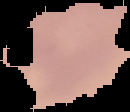
Summary:
  - Image size: 130×112 pixels
  - Preparation: thin blood smear
  - Malaria status: uninfected
  - Image type: segmented cell region on a black background